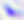

400x magnification. Toxoplasma gondii is seen. Micrograph.